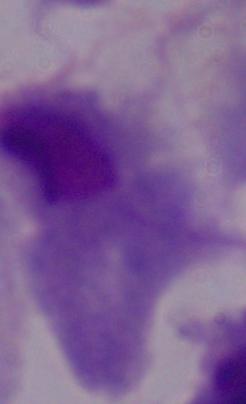
Photomicrograph. A trichomonad is seen. 1000x magnification.